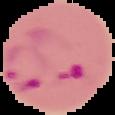 Malaria status: parasitized. Image is 115×115 pixels. The area outside the segmented cell region is set to black. From a thin blood film.